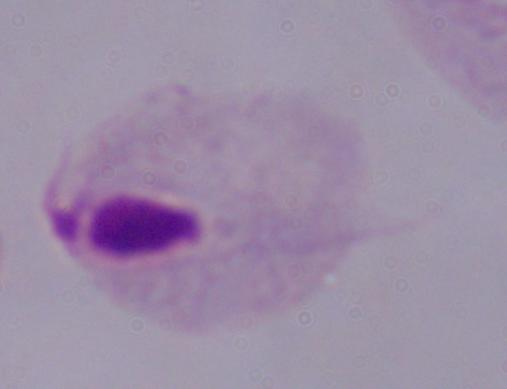 A trichomonad is shown. Captured at 1000x magnification. Micrograph.